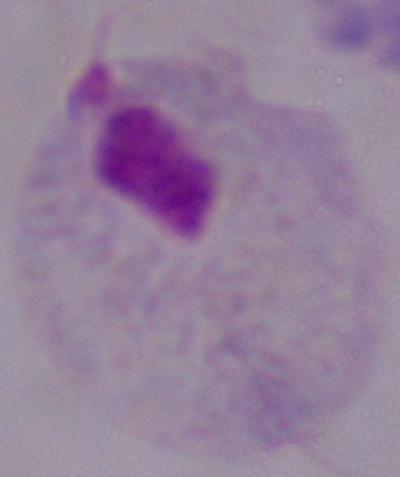

Summary:
  - Modality: photomicrograph
  - Identification: trichomonad
  - Magnification: 1000x